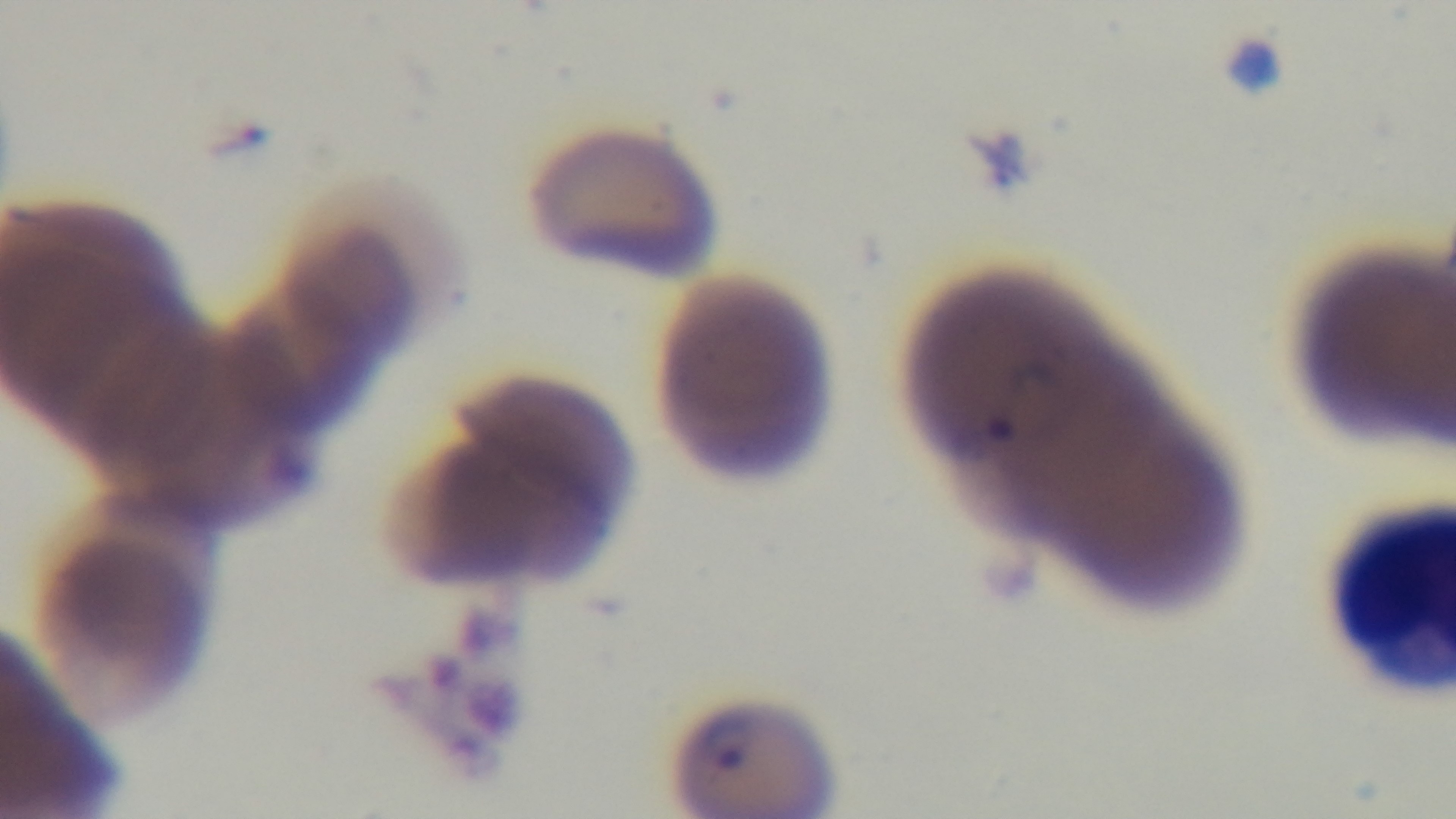 Giemsa stain. Photomicrograph. Oil-immersion objective, 100x. Preparation: thin blood film. Single field of view. Malaria status: positive. Captured with a mounted 4K digital camera.